Identify the preparation type.
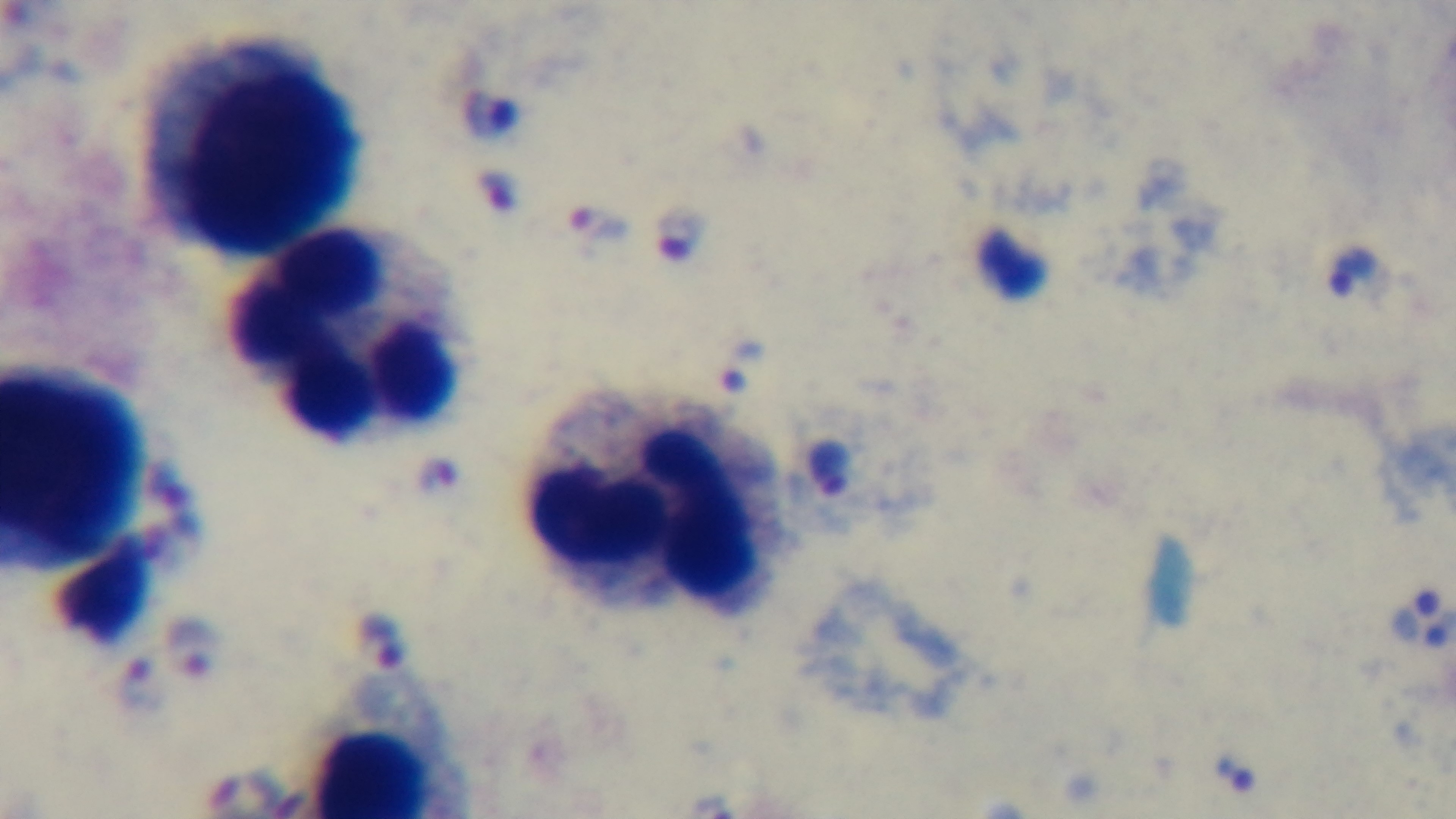

It is a thick blood film.

Giemsa stain. 100x oil-immersion objective. Captured with a mounted 4K digital camera. Malaria status: positive. Light microscopy. Single field of view.